Classify this cell by malaria status.
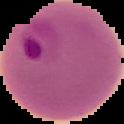
Parasitized.

Summary:
  - Preparation: thin blood film
  - Image type: segmented cell region on a black background
  - Image size: 124×124 pixels